Outline each Plasmodium falciparum-infected red blood cell.
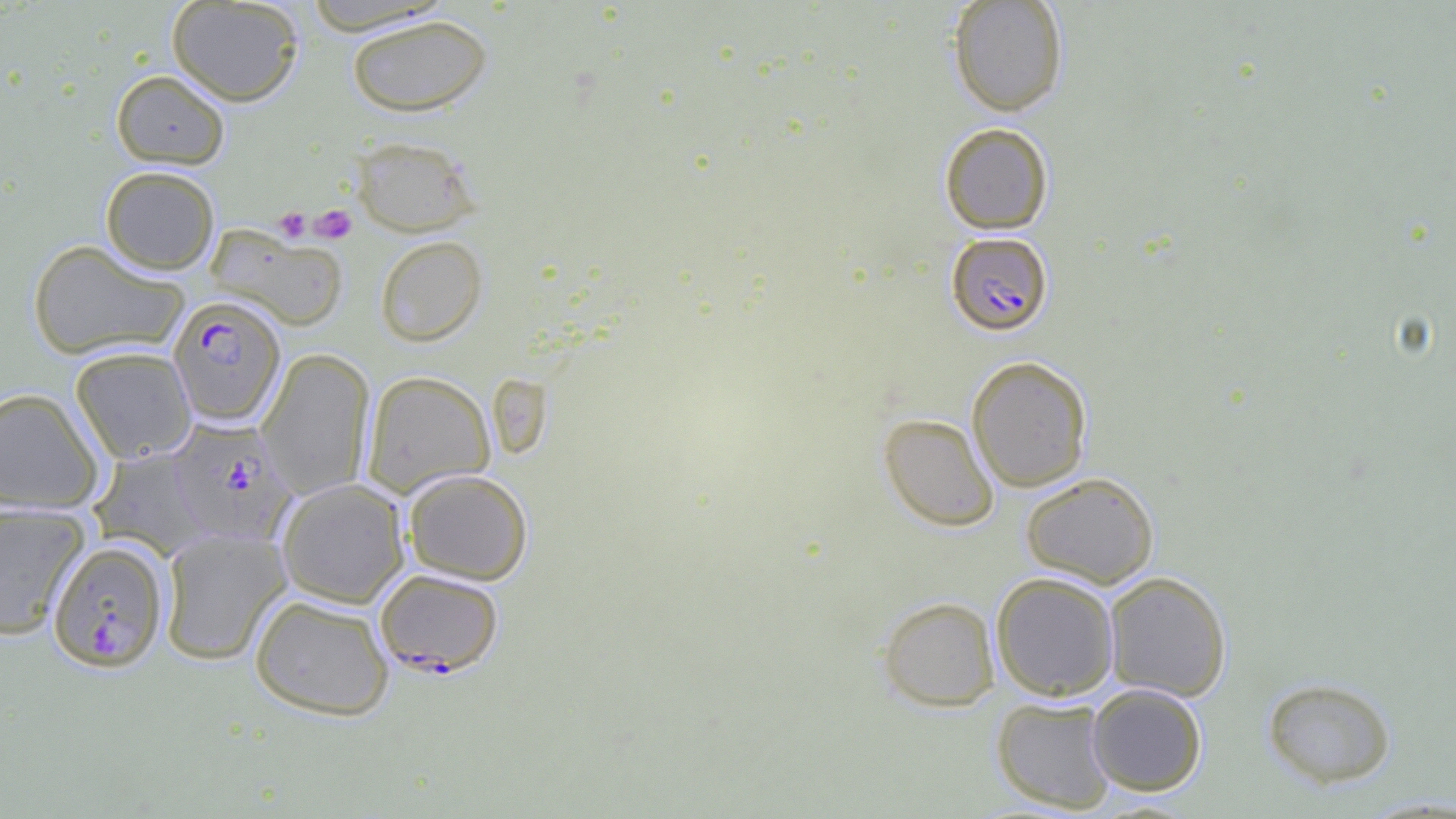
Approximate bounding boxes as [x1, y1, x2, y2] in pixels.
Plasmodium falciparum-infected red blood cells: [946, 232, 1053, 336], [167, 294, 286, 427], [166, 417, 298, 546], [47, 540, 169, 672], [375, 568, 504, 677].

Summary:
  - Uninfected red blood cell locations: [166, 0, 304, 106], [948, 0, 1069, 117], [298, 1, 456, 35], [346, 14, 492, 117], [111, 70, 230, 169], [939, 122, 1054, 234], [350, 135, 480, 237], [100, 165, 220, 274], [206, 225, 348, 331], [375, 235, 487, 346], [27, 239, 189, 360], [70, 345, 197, 463], [257, 348, 375, 499], [967, 356, 1093, 492], [362, 370, 495, 497], [0, 388, 105, 513], [879, 412, 999, 531], [89, 447, 214, 560], [403, 468, 533, 585], [1020, 472, 1159, 589], [277, 478, 409, 608], [0, 502, 90, 639], [159, 527, 291, 665], [991, 571, 1119, 701], [1103, 571, 1232, 701], [249, 594, 395, 721], [877, 595, 1000, 711], [1261, 676, 1396, 788], [1087, 684, 1207, 795], [991, 696, 1117, 813]
  - Platelet locations: [310, 204, 357, 243], [274, 207, 310, 242]
  - Slide-level diagnosis: Plasmodium falciparum
  - Preparation: thin blood smear
  - Modality: optical microscopy
  - Image size: 1456×819 pixels
  - Field of view: one of a larger specimen
  - Magnification: 1000x